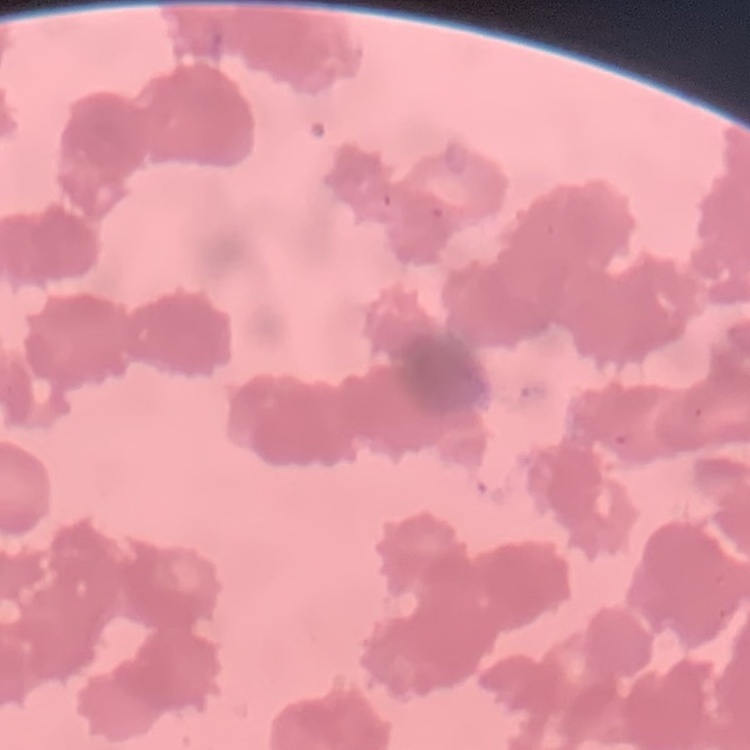 The erythrocytes exhibit rouleaux formation. Square crop of a larger photomicrograph. Field's or Giemsa stain. Thin blood smear.